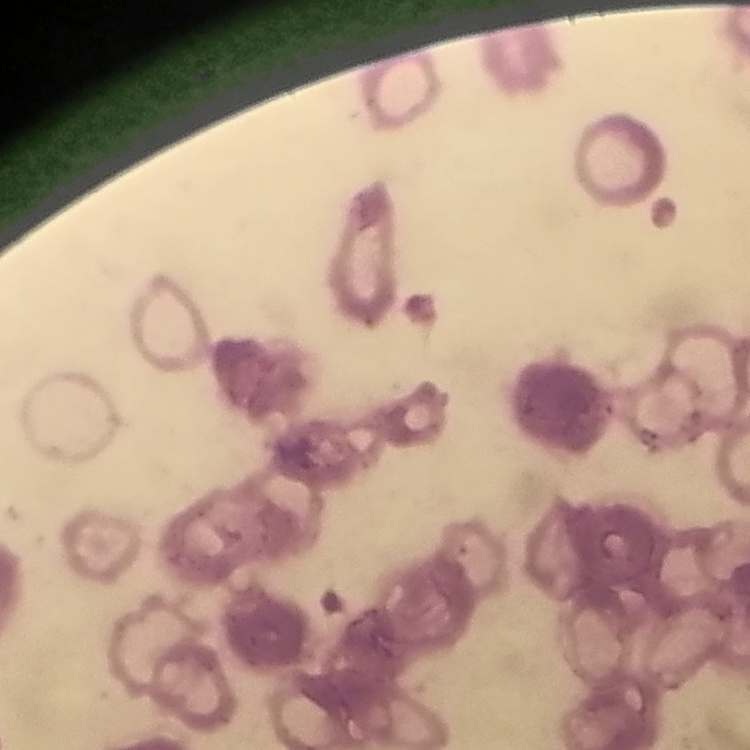

erythrocyte_morphology: rouleaux formation
preparation: thin blood smear
stain: Field's or Giemsa
image_type: square crop of a larger photomicrograph